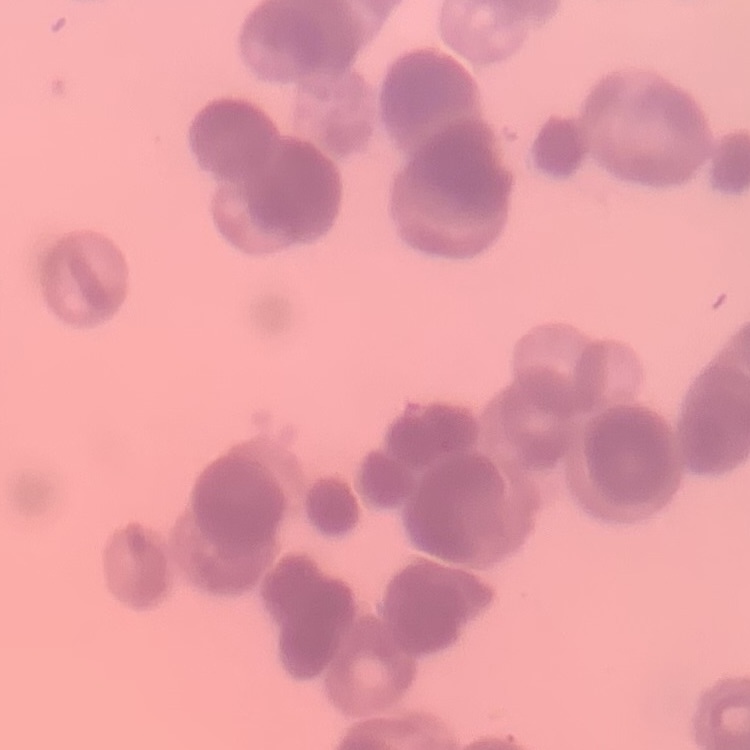

red blood cell morphology = rouleaux formation
preparation = thin blood film
stain = Field's or Giemsa
image type = square crop of a larger photomicrograph